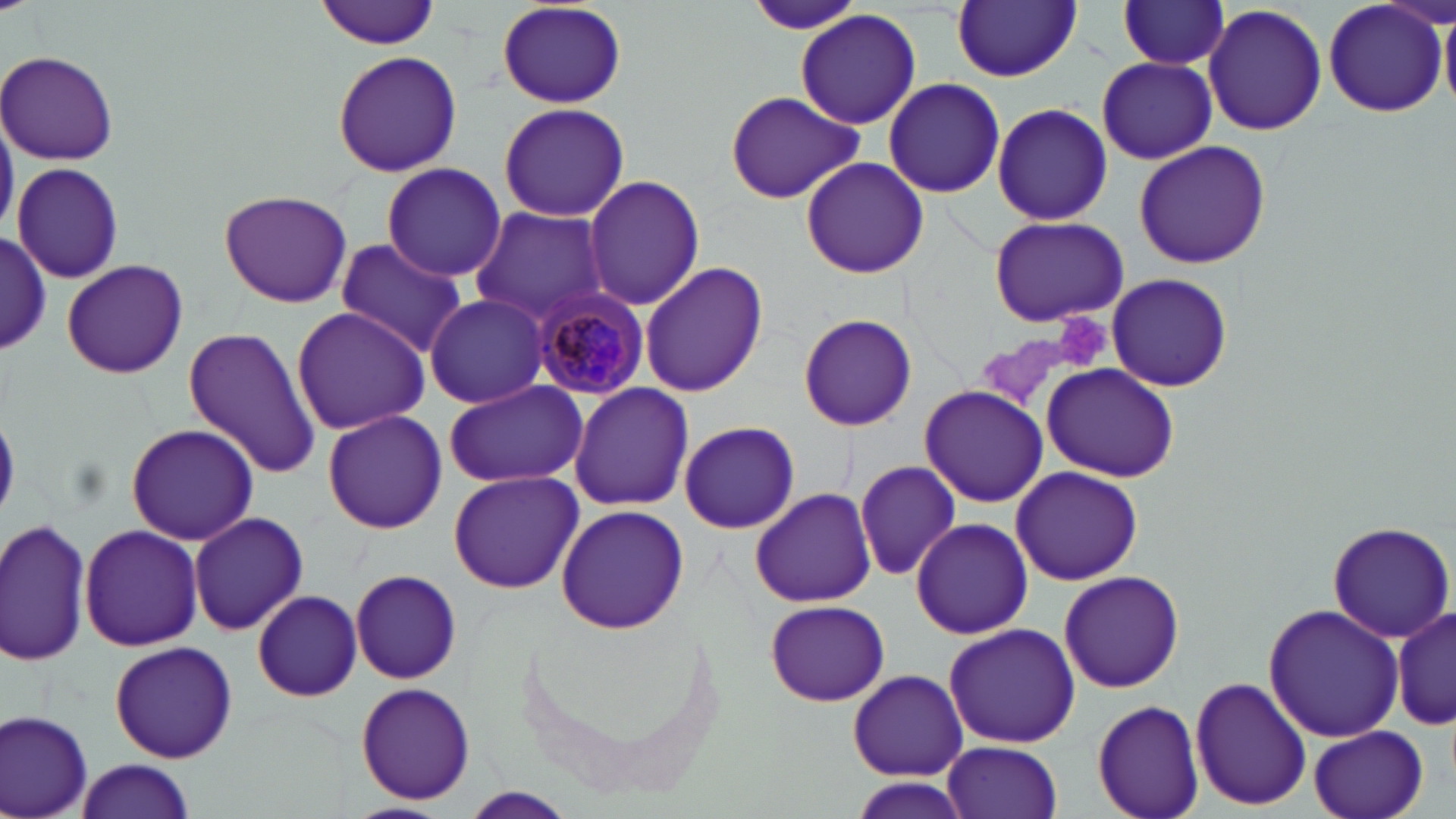

{
  "slide_level_diagnosis": "Plasmodium malariae",
  "preparation": "thin blood smear",
  "plasmodium_malariae_infected_red_blood_cell_locations": "approximate bounding boxes as (x1, y1, x2, y2) in pixels: (532, 289, 651, 399)",
  "magnification": "1000x",
  "platelet_locations": "approximate bounding boxes as (x1, y1, x2, y2) in pixels: (1061, 312, 1111, 370)",
  "image_size": "1456×819 pixels",
  "stain": "May-Grünwald-Giemsa",
  "field_of_view": "one of a larger specimen",
  "uninfected_red_blood_cell_locations": "approximate bounding boxes as (x1, y1, x2, y2) in pixels: (744, 0, 869, 35), (1116, 0, 1230, 71), (316, 1, 443, 49), (952, 1, 1080, 81), (1322, 1, 1450, 119), (494, 3, 627, 109), (1203, 4, 1328, 138), (796, 10, 920, 131), (1441, 13, 1456, 105), (332, 48, 463, 178), (1, 50, 120, 165), (1098, 57, 1216, 164), (884, 77, 1006, 198), (723, 89, 865, 203), (497, 101, 630, 222), (991, 102, 1112, 227), (1134, 140, 1271, 268), (801, 157, 926, 279), (10, 162, 123, 283), (381, 162, 507, 281), (580, 174, 707, 311), (219, 189, 352, 309), (470, 208, 608, 325), (988, 216, 1130, 328), (0, 233, 51, 353), (332, 241, 469, 358), (61, 259, 188, 379), (640, 261, 769, 398), (1106, 273, 1234, 392), (423, 293, 551, 409), (289, 306, 430, 434), (798, 314, 916, 431), (182, 326, 321, 477), (1044, 364, 1179, 479), (442, 379, 588, 489), (570, 383, 694, 512), (919, 387, 1048, 506), (323, 409, 446, 534), (677, 420, 800, 534), (125, 423, 259, 544), (854, 460, 961, 581), (1011, 467, 1143, 584), (448, 470, 584, 594), (750, 487, 878, 608), (556, 503, 690, 634), (188, 511, 307, 635), (0, 517, 91, 667), (910, 517, 1032, 640), (1328, 521, 1454, 642), (78, 524, 201, 650), (350, 570, 462, 684), (1058, 570, 1186, 692), (252, 590, 362, 701), (765, 598, 889, 706), (1263, 604, 1404, 743), (1392, 607, 1455, 732), (942, 624, 1082, 750), (108, 640, 239, 761), (849, 668, 967, 780), (1189, 675, 1312, 811), (355, 682, 477, 805), (1092, 698, 1206, 819), (2, 710, 95, 818), (1309, 725, 1431, 819), (942, 740, 1063, 819), (69, 758, 200, 818), (462, 788, 575, 817), (341, 801, 451, 819)",
  "modality": "optical microscopy"
}